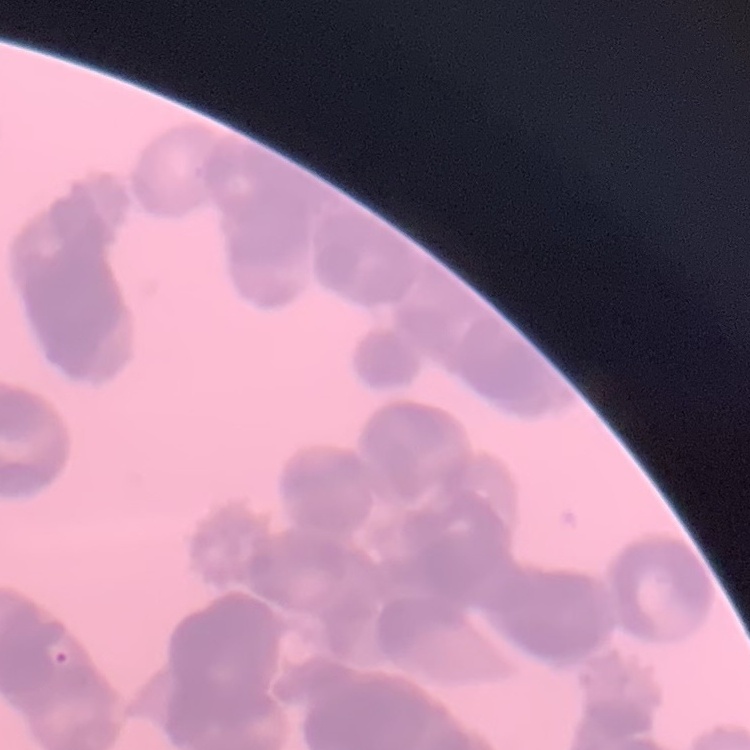

The erythrocytes exhibit rouleaux formation. One tile cut from a larger photomicrograph. Field's or Giemsa stain. Thin blood smear.